State the preparation type.
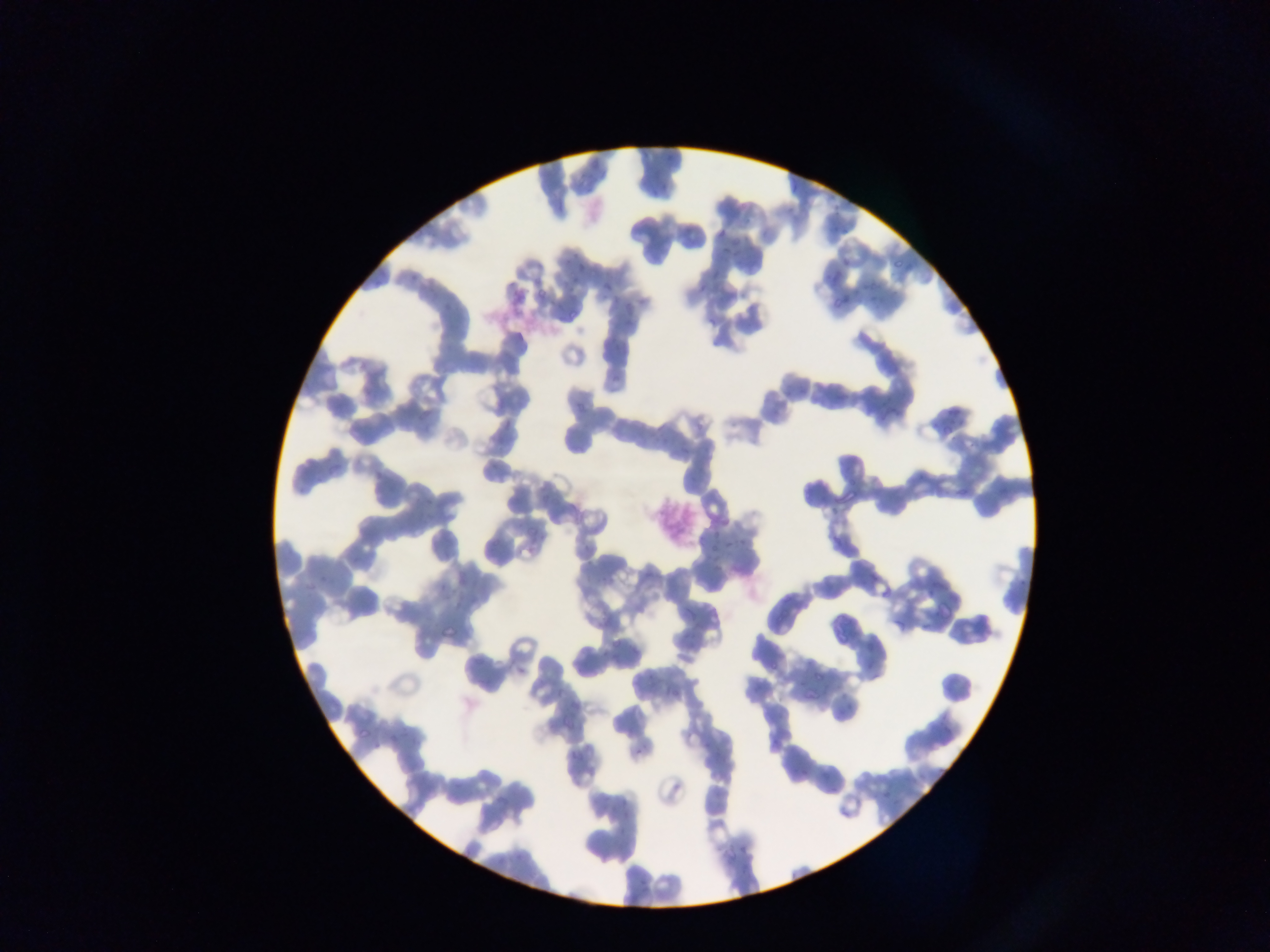

This is a thin smear.

{
  "capture": "mobile-phone photograph through a microscope",
  "artifact_stain_precipitate_or_debris_locations": "approximate bounding boxes as (left, top, right, bottom) in pixels: (492, 291, 524, 326), (652, 503, 696, 549)",
  "malaria_parasite_locations": "approximate bounding boxes as (left, top, right, bottom) in pixels: (790, 178, 802, 193), (660, 182, 668, 190), (841, 226, 850, 236), (717, 227, 724, 238), (720, 246, 734, 255), (566, 252, 577, 269), (840, 257, 852, 268), (890, 258, 902, 271), (577, 261, 587, 270), (570, 276, 578, 281), (698, 282, 708, 290), (601, 284, 610, 293), (536, 289, 546, 298), (870, 291, 881, 303), (831, 298, 844, 306), (567, 307, 578, 319), (705, 316, 713, 325), (610, 372, 623, 384), (798, 386, 810, 395), (945, 405, 956, 415), (711, 528, 720, 539), (738, 539, 748, 547), (722, 540, 732, 546), (708, 544, 718, 553), (868, 573, 878, 582), (927, 588, 938, 598), (877, 590, 888, 600), (894, 618, 902, 629), (442, 622, 459, 639), (770, 657, 779, 669), (517, 662, 528, 674), (812, 668, 822, 680), (846, 702, 855, 711), (357, 724, 374, 741), (771, 738, 781, 746), (635, 747, 646, 754), (799, 766, 808, 779), (826, 783, 838, 791), (739, 847, 749, 854), (639, 877, 646, 887) | approximate (x, y) pixel centers of objects too small to bound: (655, 194), (748, 222), (926, 626)",
  "country": "Ghana",
  "field_of_view": "single",
  "image_size": "1270×952 pixels"
}